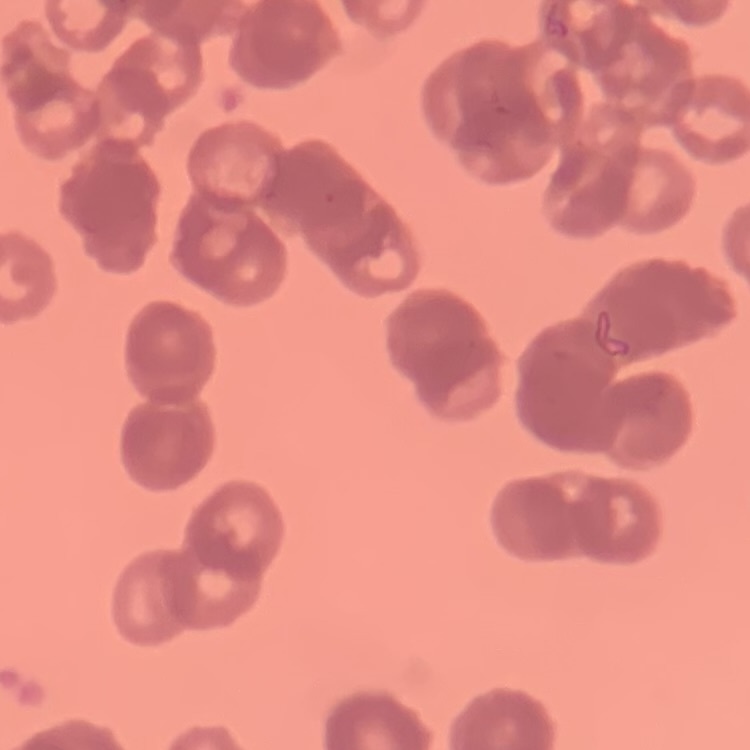

Summary:
  - Red blood cell morphology: rouleaux formation
  - Stain: Field's or Giemsa
  - Image type: square crop of a larger photomicrograph
  - Preparation: thin blood smear